Classify this cell by malaria status.
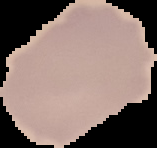
It is uninfected.

The area outside the segmented cell region is set to black. From a thin blood film. Image is 157×148 pixels.